Classify this cell by malaria status.
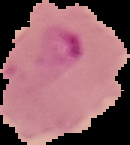

Parasitized.

image type = segmented cell region on a black background
preparation = thin blood film
image size = 130×145 pixels